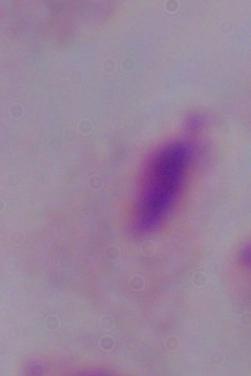
Summary:
  - Magnification: 1000x
  - Modality: micrograph
  - Identification: trichomonad